Point out each malaria parasite.
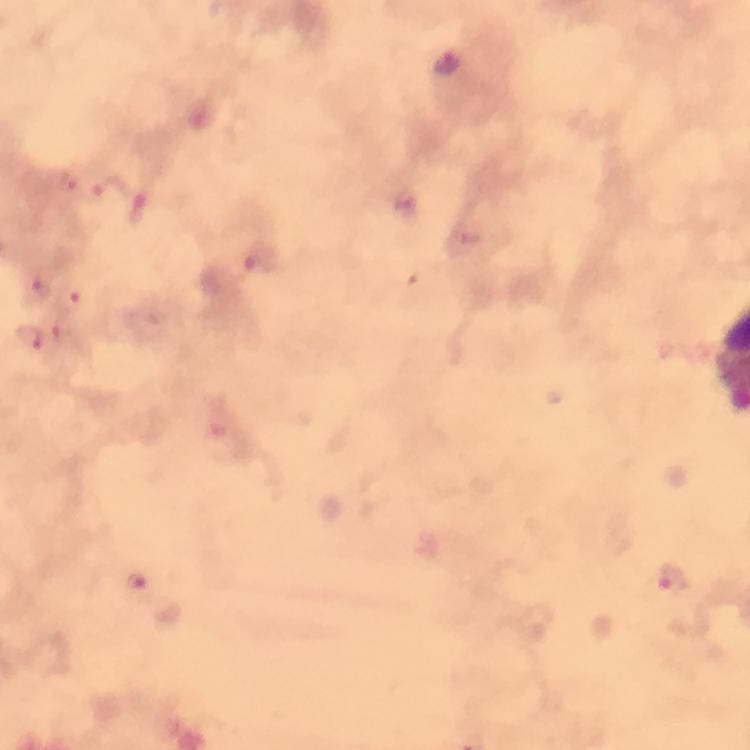

Approximate centers as [x, y] in pixels.
Malaria parasites: [449, 62], [69, 188], [110, 188], [405, 203], [139, 212], [472, 234], [259, 266], [40, 289], [71, 295], [30, 338], [69, 342], [674, 579], [135, 583].

stain = Giemsa
context = from a malaria diagnostic workup
cropped from = a single field of view
preparation = thick blood smear
image size = 750×750 pixels
capture = smartphone camera through the microscope
immersion oil = applied
magnification = 100x